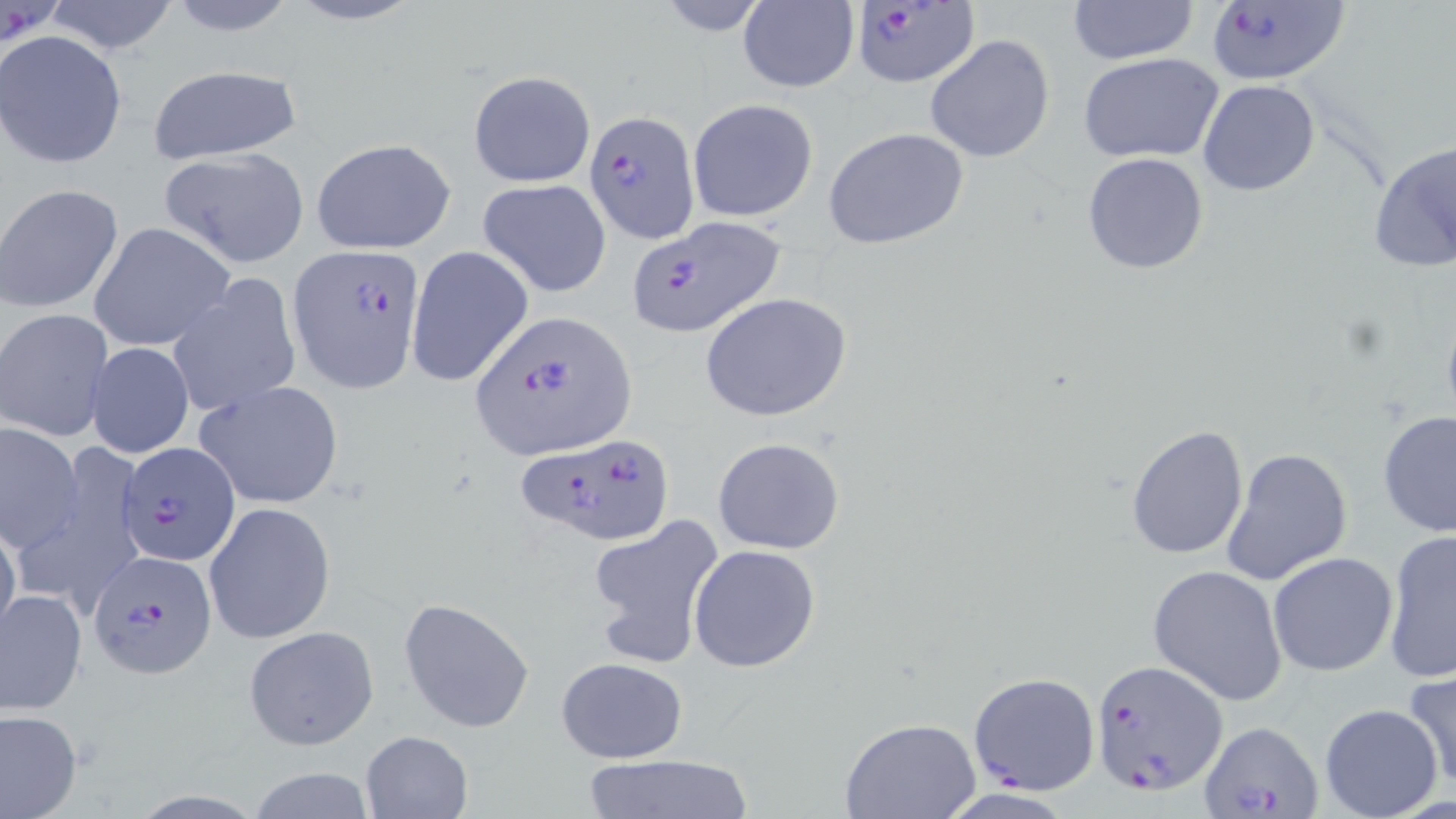

Approximate bounding boxes as named x1/y1/x2/y2 corners in pixels. Uninfected red blood cell locations: (x1=44, y1=0, x2=181, y2=56), (x1=281, y1=0, x2=427, y2=27), (x1=651, y1=0, x2=777, y2=35), (x1=163, y1=1, x2=302, y2=37), (x1=1065, y1=1, x2=1202, y2=65), (x1=737, y1=2, x2=859, y2=92), (x1=0, y1=31, x2=128, y2=167), (x1=924, y1=34, x2=1056, y2=161), (x1=1079, y1=54, x2=1224, y2=164), (x1=143, y1=64, x2=302, y2=165), (x1=467, y1=69, x2=596, y2=187), (x1=1197, y1=79, x2=1320, y2=197), (x1=686, y1=98, x2=819, y2=223), (x1=823, y1=127, x2=970, y2=250), (x1=310, y1=136, x2=457, y2=255), (x1=1368, y1=139, x2=1455, y2=274), (x1=159, y1=147, x2=310, y2=268), (x1=1082, y1=152, x2=1210, y2=275), (x1=477, y1=177, x2=613, y2=298), (x1=0, y1=184, x2=124, y2=314), (x1=89, y1=223, x2=233, y2=351), (x1=406, y1=246, x2=533, y2=387), (x1=167, y1=274, x2=302, y2=418), (x1=699, y1=292, x2=852, y2=421), (x1=0, y1=308, x2=115, y2=441), (x1=85, y1=342, x2=195, y2=458), (x1=193, y1=381, x2=344, y2=510), (x1=1377, y1=409, x2=1456, y2=537), (x1=0, y1=424, x2=83, y2=554), (x1=1125, y1=424, x2=1250, y2=560), (x1=713, y1=436, x2=845, y2=555), (x1=30, y1=442, x2=148, y2=611), (x1=1219, y1=446, x2=1353, y2=587), (x1=205, y1=501, x2=336, y2=642), (x1=587, y1=513, x2=725, y2=667), (x1=0, y1=517, x2=21, y2=648), (x1=1382, y1=527, x2=1455, y2=683), (x1=689, y1=544, x2=821, y2=671), (x1=1267, y1=552, x2=1399, y2=676), (x1=1147, y1=563, x2=1288, y2=705), (x1=1, y1=589, x2=87, y2=713), (x1=397, y1=598, x2=535, y2=734), (x1=242, y1=626, x2=380, y2=750), (x1=555, y1=657, x2=689, y2=763), (x1=1403, y1=669, x2=1456, y2=797), (x1=1319, y1=702, x2=1444, y2=819), (x1=1, y1=708, x2=83, y2=818), (x1=839, y1=718, x2=982, y2=819), (x1=361, y1=730, x2=473, y2=818), (x1=584, y1=753, x2=756, y2=819), (x1=246, y1=764, x2=375, y2=819). Plasmodium falciparum-infected red blood cell locations: (x1=848, y1=0, x2=979, y2=90), (x1=1204, y1=0, x2=1354, y2=88), (x1=585, y1=109, x2=700, y2=243), (x1=626, y1=217, x2=783, y2=337), (x1=288, y1=245, x2=425, y2=391), (x1=470, y1=312, x2=636, y2=458), (x1=515, y1=433, x2=676, y2=548), (x1=117, y1=439, x2=242, y2=569), (x1=87, y1=549, x2=217, y2=677), (x1=1090, y1=658, x2=1227, y2=796), (x1=967, y1=672, x2=1101, y2=795), (x1=1198, y1=719, x2=1325, y2=817). Slide-level diagnosis: Plasmodium falciparum. Image is 1456×819 pixels. May-Grünwald-Giemsa stain. Light microscopy. Thin blood smear. Single field of view. 1000x magnification.